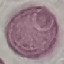
Summary:
  - Result: no malaria parasites detected
  - Image type: automatically extracted cell patch, resized to 64 × 64 pixels
  - Preparation: thin blood smear
  - Stain: Giemsa
  - Capture: smartphone through the microscope eyepiece